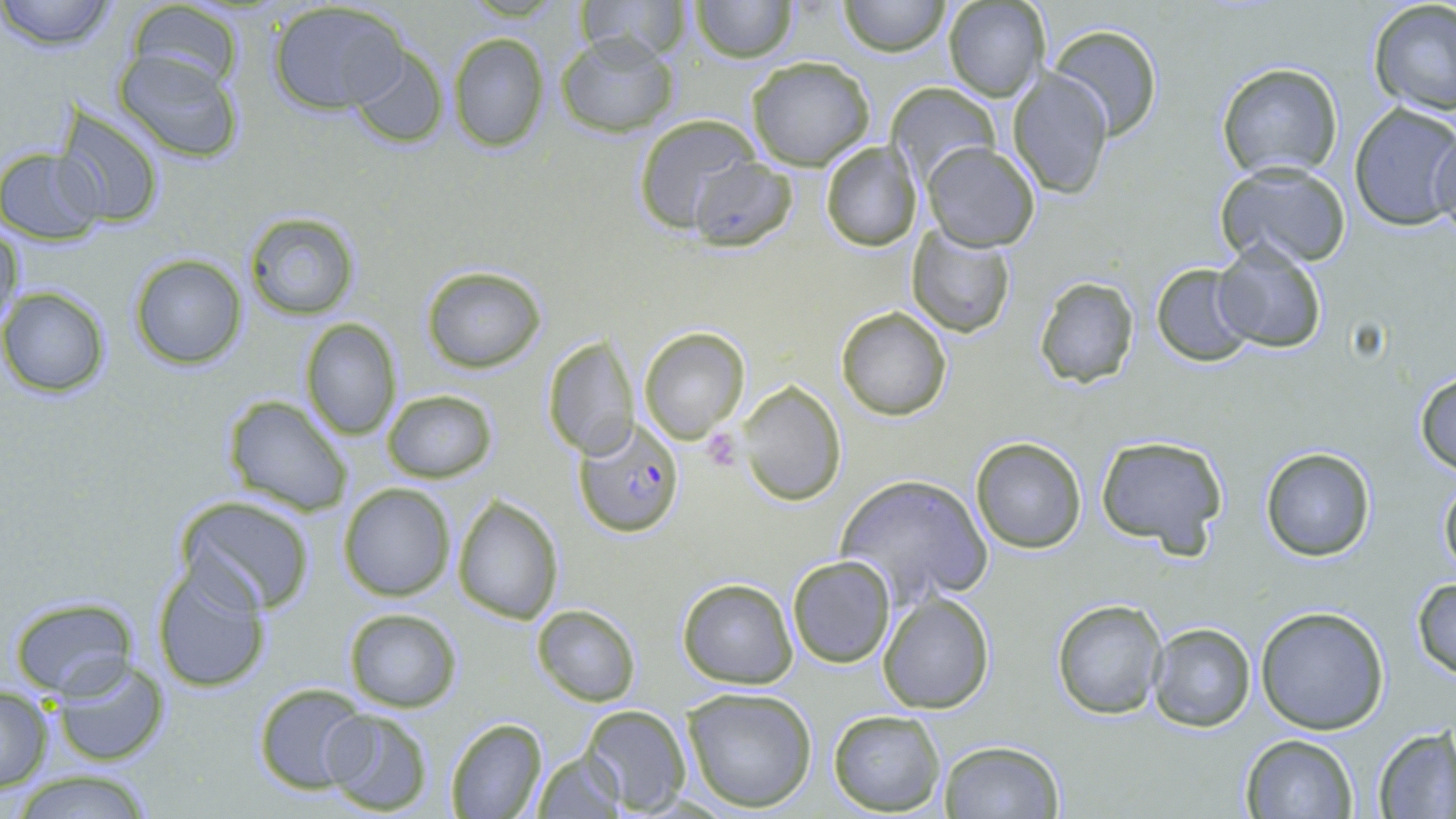
Summary:
  - Coordinate format: approximate bounding boxes as (x1, y1, x2, y2) in pixels
  - Plasmodium falciparum-infected red blood cell locations: (571, 416, 687, 538)
  - Platelet locations: (700, 426, 745, 473)
  - Uninfected red blood cell locations: (0, 0, 117, 49), (573, 0, 694, 64), (689, 0, 797, 63), (838, 0, 951, 56), (125, 1, 248, 96), (942, 1, 1048, 102), (1365, 1, 1456, 117), (266, 2, 410, 116), (1045, 23, 1165, 141), (445, 32, 551, 153), (554, 33, 681, 138), (346, 45, 451, 150), (111, 48, 245, 163), (745, 55, 877, 171), (1215, 60, 1344, 181), (1007, 66, 1113, 199), (886, 82, 1002, 189), (1347, 102, 1456, 234), (53, 108, 165, 229), (631, 112, 758, 234), (1427, 122, 1456, 245), (821, 140, 922, 252), (922, 142, 1040, 252), (1, 147, 105, 243), (687, 156, 800, 252), (1214, 161, 1354, 271), (242, 211, 361, 319), (0, 220, 22, 337), (905, 225, 1017, 339), (1215, 244, 1329, 354), (128, 253, 247, 370), (1151, 263, 1256, 366), (420, 266, 548, 372), (1032, 275, 1140, 388), (2, 287, 113, 397), (836, 307, 954, 421), (300, 318, 403, 439), (640, 327, 750, 443), (542, 334, 639, 459), (1412, 370, 1456, 474), (738, 382, 847, 505), (381, 389, 498, 483), (221, 394, 353, 516), (1093, 433, 1229, 553), (969, 435, 1087, 554), (1259, 446, 1376, 562), (836, 472, 993, 606), (1438, 477, 1456, 578), (338, 482, 456, 601), (172, 494, 318, 616), (452, 494, 563, 624), (787, 554, 895, 669), (151, 562, 270, 694), (676, 575, 799, 690), (1410, 577, 1456, 681), (6, 593, 141, 702), (878, 593, 995, 715), (1051, 597, 1167, 719), (532, 603, 640, 707), (1255, 605, 1390, 735), (343, 607, 463, 712), (1148, 620, 1257, 733), (49, 657, 173, 768), (251, 680, 369, 794), (681, 687, 817, 813), (0, 688, 52, 791), (582, 704, 690, 815), (321, 707, 433, 816), (827, 708, 945, 816), (445, 717, 548, 819), (1372, 727, 1454, 818), (1241, 734, 1359, 819), (938, 741, 1064, 819), (533, 750, 625, 817), (8, 770, 159, 819)
  - Slide-level diagnosis: Plasmodium falciparum
  - Modality: light microscopy
  - Image size: 1456×819 pixels
  - Field of view: one of a larger specimen
  - Stain: May-Grünwald-Giemsa
  - Preparation: thin blood film
  - Magnification: 1000x